Name the parasite shown.
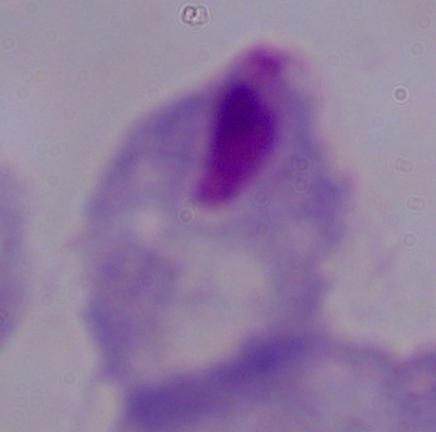

A trichomonad.

modality = photomicrograph
magnification = 1000x